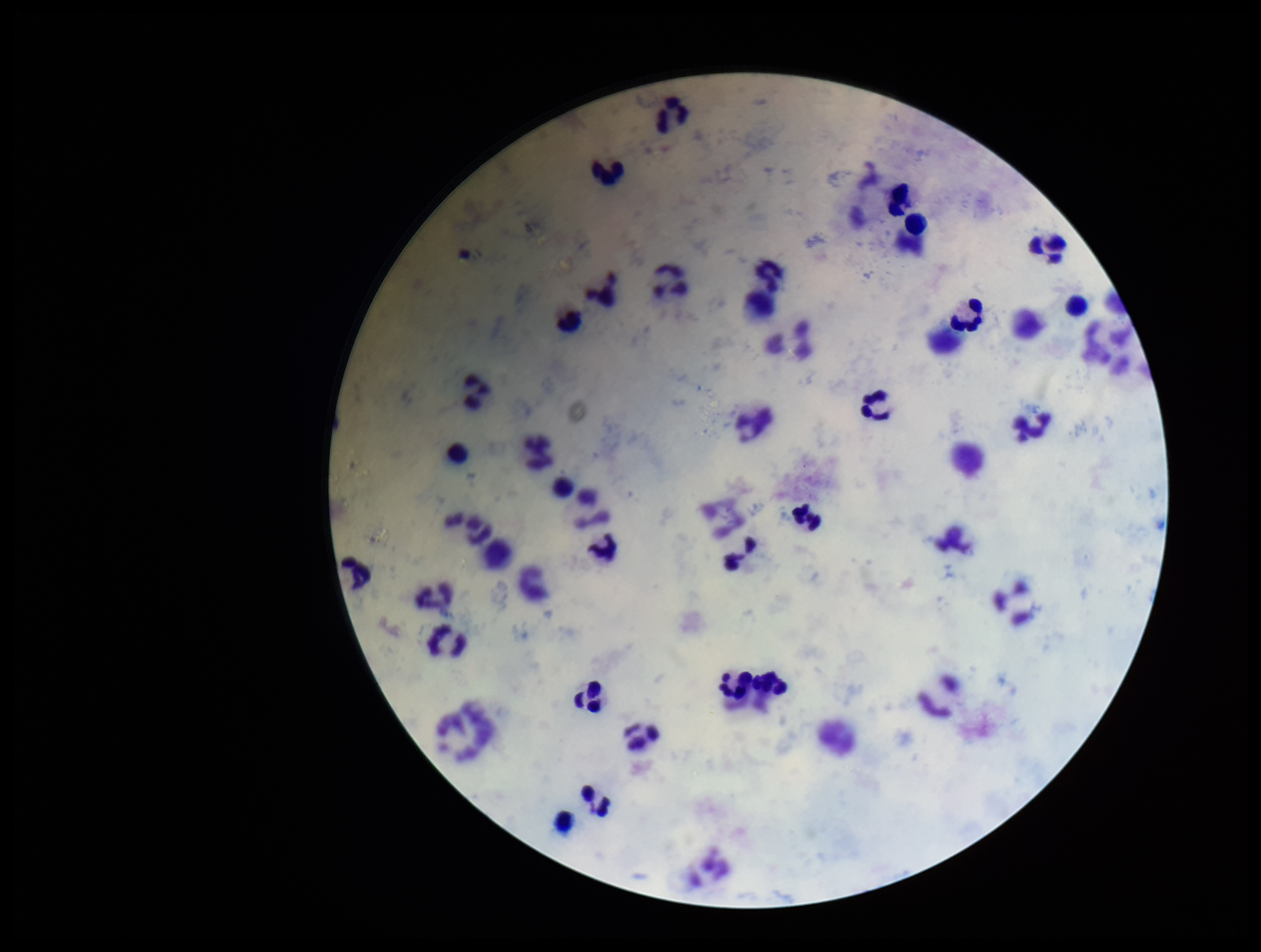 Stained with Giemsa. Image is 1261×952 pixels. Plasmodium parasites: none detected. Patient malaria status: negative. Photographed through the microscope eyepiece with a smartphone camera. One field from this slide. Parasite count: 0. Leukocyte count: 51. Preparation: thick.